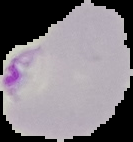

Image is 133×142 pixels. Segmented cell region on a black background. Result: Plasmodium parasites identified. From a thin blood film.